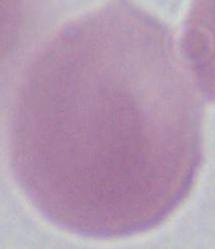

Summary:
  - Identification: erythrocyte
  - Magnification: 1000x
  - Modality: micrograph